Point out each Plasmodium parasite.
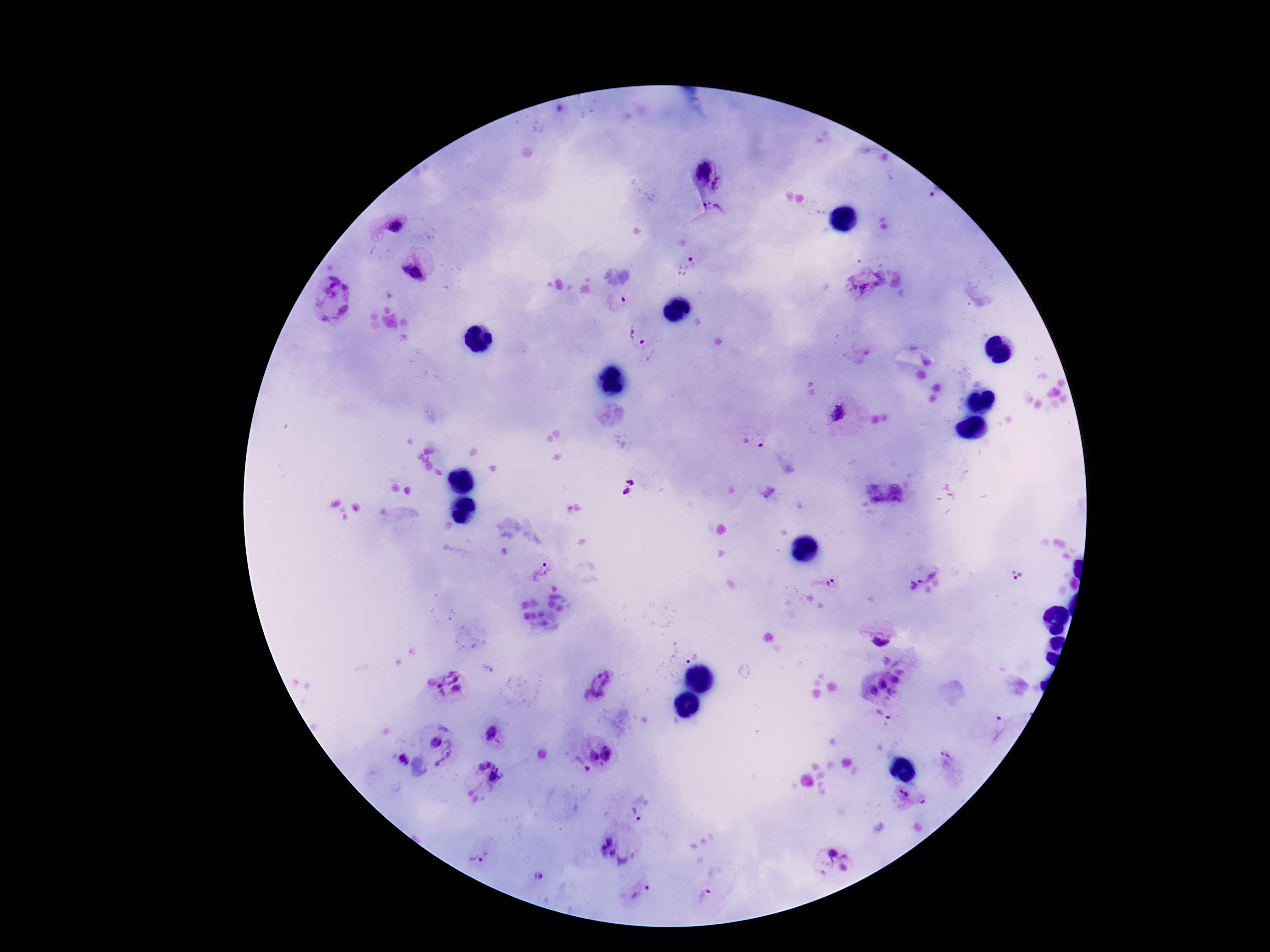

Approximate centers as (x, y) in pixels.
Plasmodium parasites: (703, 170), (717, 183), (712, 208), (395, 224), (690, 259), (412, 271), (867, 278), (328, 298), (618, 299), (637, 335), (839, 413), (756, 441), (627, 485), (541, 570), (923, 576), (1016, 576), (831, 582), (879, 637), (899, 660), (895, 680), (598, 683), (882, 684), (452, 685), (872, 689), (893, 692), (1002, 727), (490, 733), (436, 741), (607, 751), (442, 753), (594, 756), (945, 757), (402, 760), (483, 764), (602, 764), (587, 769), (497, 775), (904, 793), (639, 812), (615, 847), (831, 853), (846, 856), (476, 859), (844, 867), (538, 876), (642, 891), (705, 896).

Giemsa-stained preparation. Thick peripheral-blood smear. Single field of view. Patient malaria status: positive. Image is 1270×952 pixels. Smartphone photograph taken through the microscope eyepiece. 100x magnification.